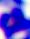
modality = photomicrograph
magnification = 400x
identification = white blood cell